Locate every malaria parasite.
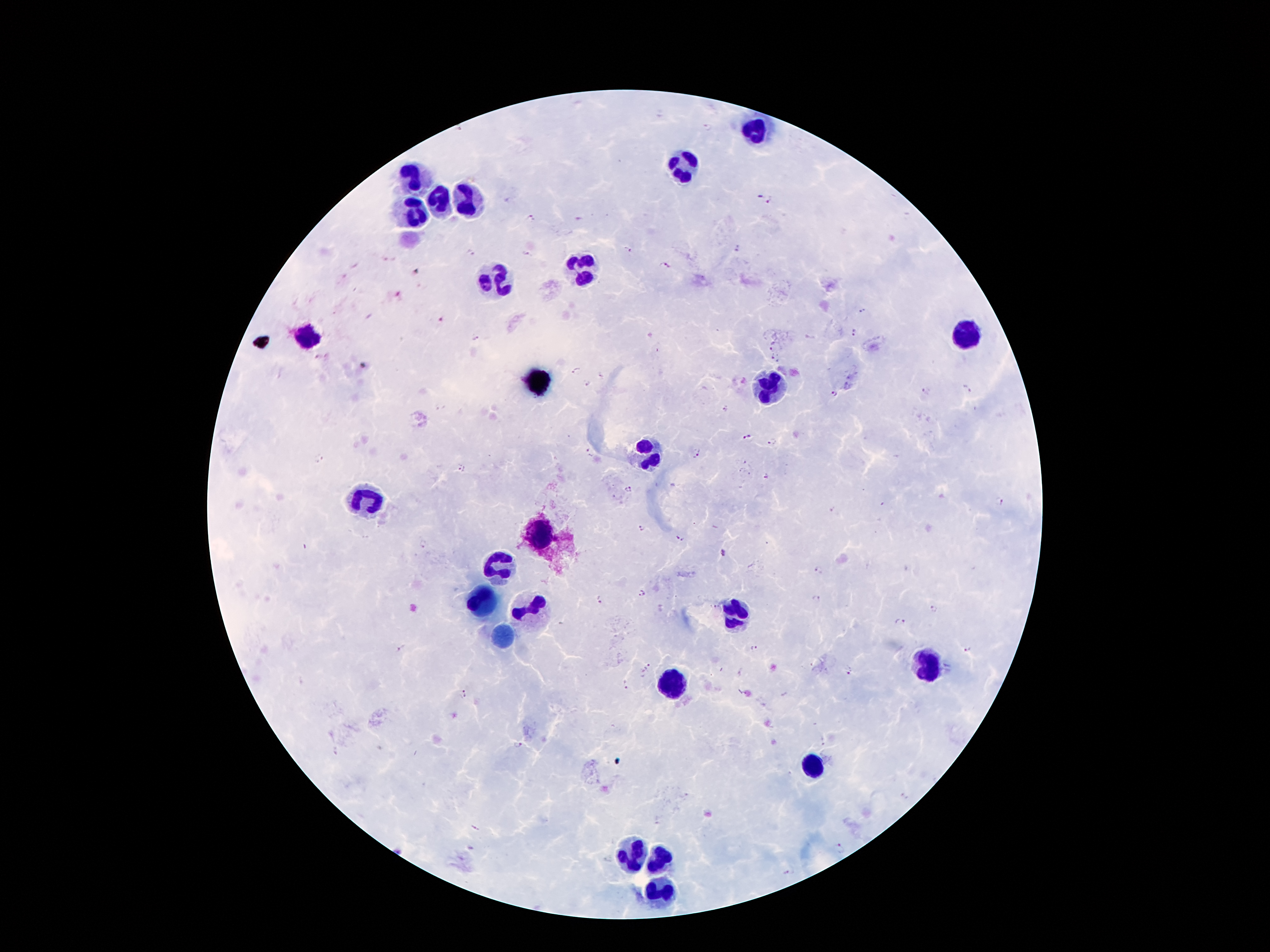

Approximate centers as [x, y] in pixels.
Malaria parasites: [706, 127], [760, 196], [770, 201], [530, 216], [580, 219], [737, 249], [627, 250], [471, 252], [527, 254], [666, 266], [417, 271], [400, 295], [862, 311], [438, 323], [854, 333], [478, 339], [773, 347], [317, 356], [775, 356], [576, 369], [602, 375], [588, 384], [967, 388], [925, 390], [833, 393], [725, 408], [745, 436], [772, 442], [587, 453], [696, 453], [318, 458], [462, 467], [765, 476], [628, 489], [999, 502], [833, 510], [642, 528], [680, 537], [424, 543], [723, 554], [817, 570], [641, 592], [817, 598], [602, 600], [715, 606], [934, 609], [901, 622], [754, 648], [968, 648], [400, 649], [648, 667], [849, 673], [626, 684], [461, 693], [822, 739], [516, 743], [476, 827], [840, 847], [788, 872].

Leukocyte locations: [755, 130], [682, 166], [411, 170], [442, 202], [468, 202], [411, 214], [583, 273], [495, 282], [963, 330], [304, 338], [770, 391], [652, 447], [365, 504], [539, 536], [499, 571], [482, 599], [531, 605], [734, 611], [930, 662], [671, 685], [810, 771], [633, 853], [652, 859], [657, 891]. Giemsa-stained preparation. 100x magnification. Patient malaria status: positive for Plasmodium falciparum. One field from this slide. Photographed through the microscope eyepiece with a smartphone camera. Image is 1270×952 pixels. Thick blood smear.